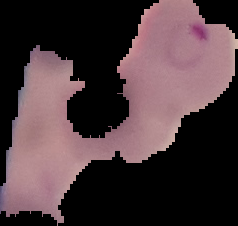

Summary:
  - Image size: 238×226 pixels
  - Preparation: thin blood film
  - Result: malaria parasites detected
  - Image type: cell region segmented out of the field of view; surrounding area masked to black